Report the malaria status of this cell.
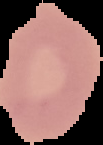
It is uninfected.

Summary:
  - Image type: cell region segmented out of the field of view; surrounding area masked to black
  - Image size: 103×145 pixels
  - Preparation: thin blood smear